Classify this cell by malaria status.
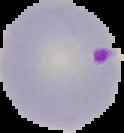

It is parasitized.

image type = segmented cell region on a black background
preparation = thin blood smear
image size = 124×133 pixels